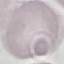
result: no malaria parasites seen
capture: smartphone camera at the microscope eyepiece
stain: Giemsa
image_type: cell patch, automatically extracted from a larger field of view and resized to 64 × 64 pixels
preparation: thin blood film